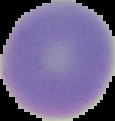
Summary:
  - Image type: segmented cell region on a black background
  - Preparation: thin blood smear
  - Result: negative for Plasmodium parasites
  - Image size: 115×121 pixels